Point out malaria parasites and leukocytes.
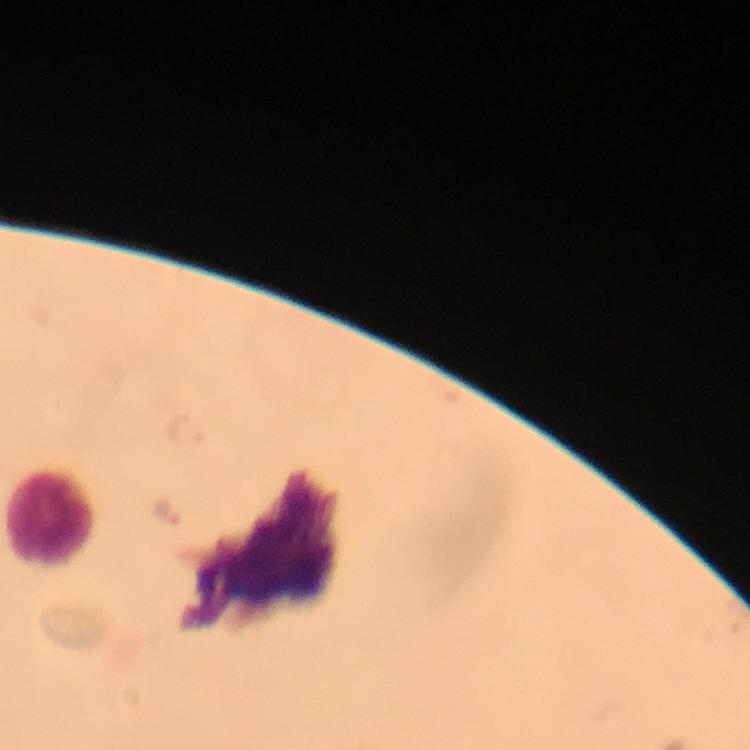

Approximate object centers, in pixels from the top-left corner.
Malaria parasites: (x=187, y=431), (x=167, y=510).
Leukocytes: (x=51, y=517).

Giemsa-stained preparation. 100x magnification. A crop from one field of view. Image is 750×750 pixels. Photographed through the microscope with a smartphone camera. From a diagnostic examination for malaria. Thick blood film. Immersion oil was used.